Locate every blood parasite and identify its species.
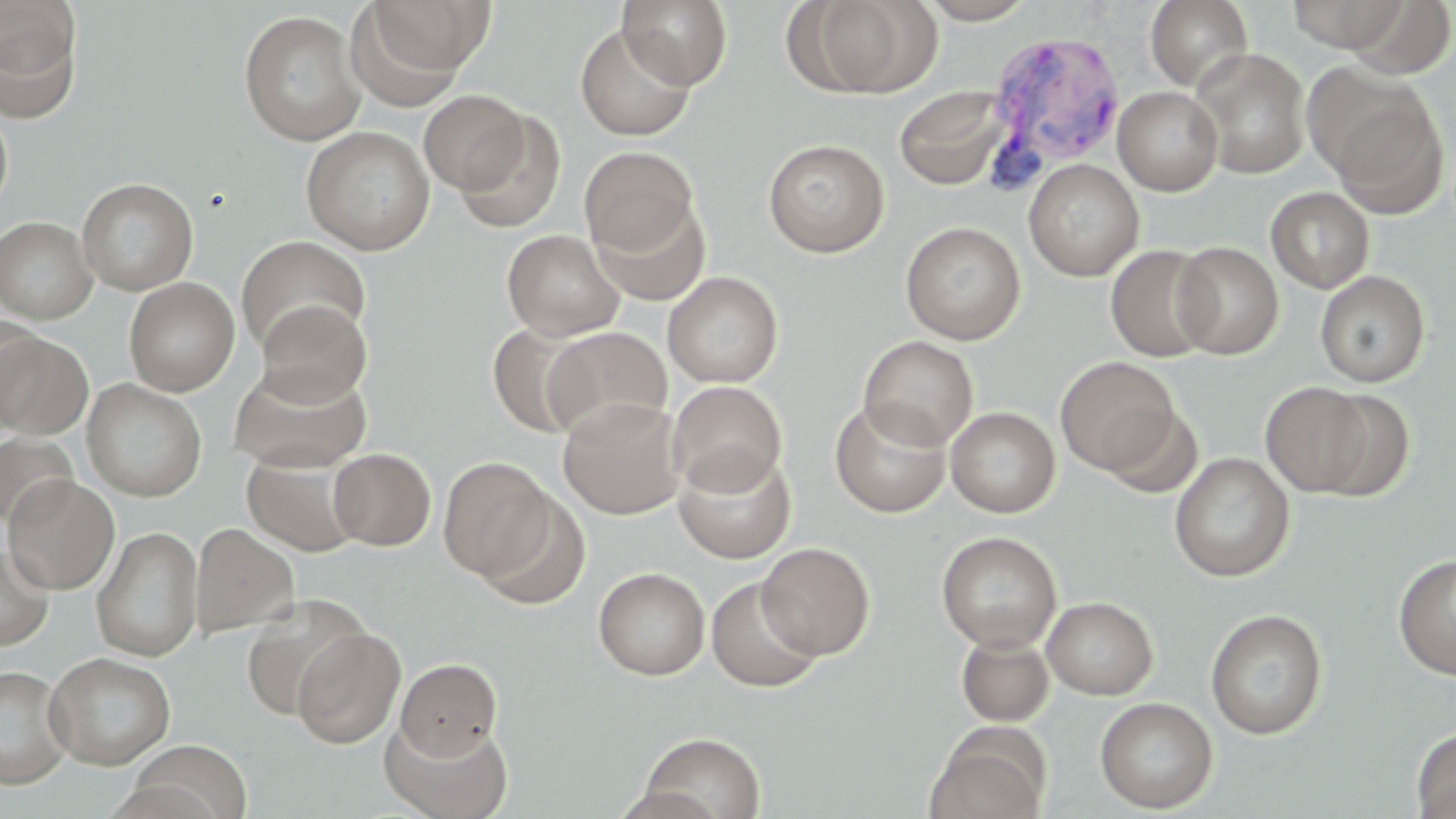

Approximate bounding boxes as (x1,y1)-(x2,y2) corner pairs in pixels.
Plasmodium vivax-infected red blood cells: (983,29)-(1126,187).
No Plasmodium falciparum, Plasmodium ovale, Plasmodium malariae, Babesia divergens, or Trypanosoma brucei observed.

slide-level diagnosis = Plasmodium vivax
field of view = one of a larger specimen
image size = 1456×819 pixels
preparation = thin blood smear
modality = optical microscopy
magnification = 1000x
stain = May-Grünwald-Giemsa
uninfected red blood cell locations = approximate bounding boxes as (x1,y1)-(x2,y2) corner pairs in pixels: (355,0)-(495,87), (617,0)-(733,90), (797,0)-(939,98), (918,0)-(1037,24), (1145,0)-(1253,91), (1283,0)-(1417,54), (0,1)-(83,120), (238,10)-(368,147), (574,23)-(696,142), (1190,48)-(1312,180), (1318,82)-(1449,218), (1113,85)-(1224,196), (894,86)-(1010,190), (419,89)-(530,195), (0,106)-(13,216), (452,109)-(567,235), (301,125)-(435,255), (763,138)-(889,258), (579,146)-(698,257), (1023,159)-(1144,281), (77,177)-(199,296), (1265,187)-(1375,293), (591,197)-(710,306), (0,215)-(98,323), (901,221)-(1026,345), (502,229)-(625,341), (235,235)-(370,355), (1172,241)-(1284,359), (1105,244)-(1219,362), (1315,270)-(1430,388), (662,271)-(783,388), (124,277)-(240,396), (256,300)-(372,405), (0,316)-(41,421), (489,325)-(591,438), (542,327)-(671,440), (0,332)-(94,439), (859,335)-(979,450), (1055,356)-(1179,475), (228,364)-(372,472), (82,378)-(207,502), (667,381)-(786,495), (1260,381)-(1374,496), (1309,388)-(1415,501), (557,397)-(686,519), (830,399)-(951,518), (1103,405)-(1203,499), (946,406)-(1060,518), (0,432)-(77,530), (674,446)-(797,564), (328,448)-(435,550), (242,452)-(363,557), (1169,452)-(1294,582), (438,455)-(554,582), (3,474)-(120,594), (476,489)-(593,612), (189,522)-(299,638), (91,525)-(204,662), (936,531)-(1062,652), (756,542)-(875,659), (0,543)-(55,651), (1393,554)-(1456,680), (593,567)-(710,680), (706,576)-(824,693), (239,594)-(369,718), (1042,596)-(1159,700), (1206,609)-(1328,739), (292,626)-(405,749), (956,633)-(1055,727), (44,652)-(176,771), (396,658)-(502,760), (0,664)-(74,790), (1095,697)-(1218,813), (380,716)-(513,819), (927,727)-(1048,819), (1411,727)-(1456,818), (637,731)-(766,819), (128,740)-(253,819)